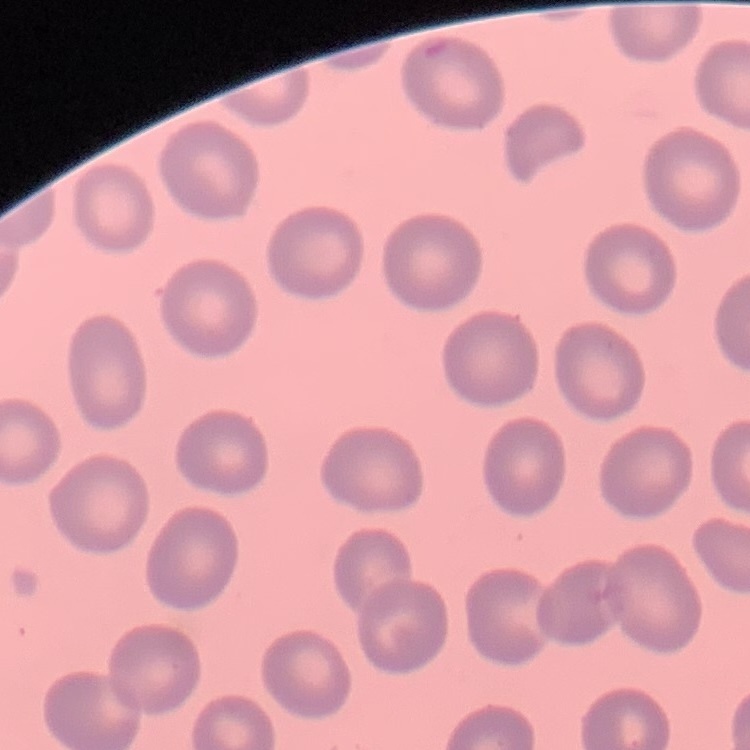 The red blood cells exhibit no rouleaux formation. One tile cut from a larger photomicrograph. Thin peripheral smear. Stained with either Field's or Giemsa.